Comment on the morphology of the erythrocytes.
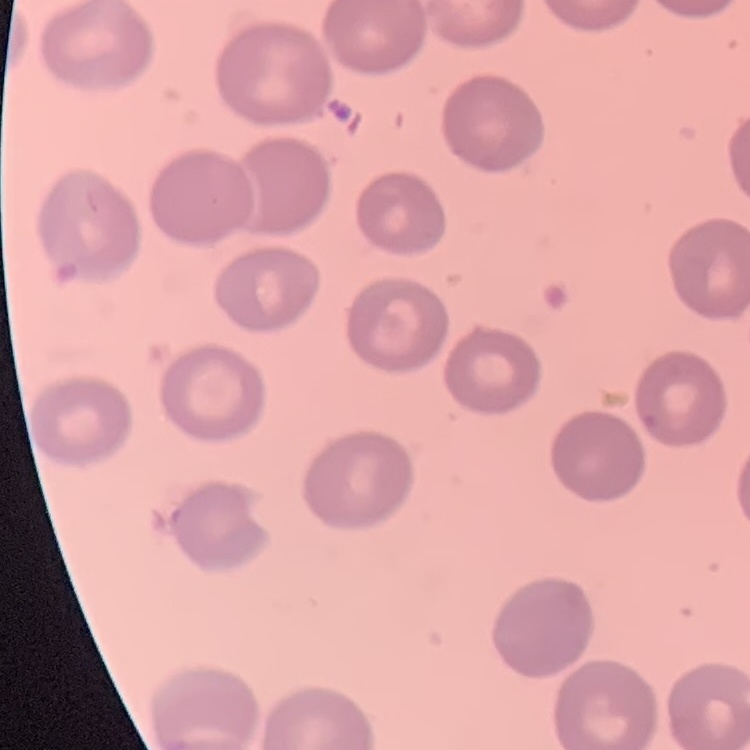
They show no rouleaux formation.

Summary:
  - Stain: Field's or Giemsa
  - Preparation: thin blood film
  - Image type: one tile cut from a larger photomicrograph